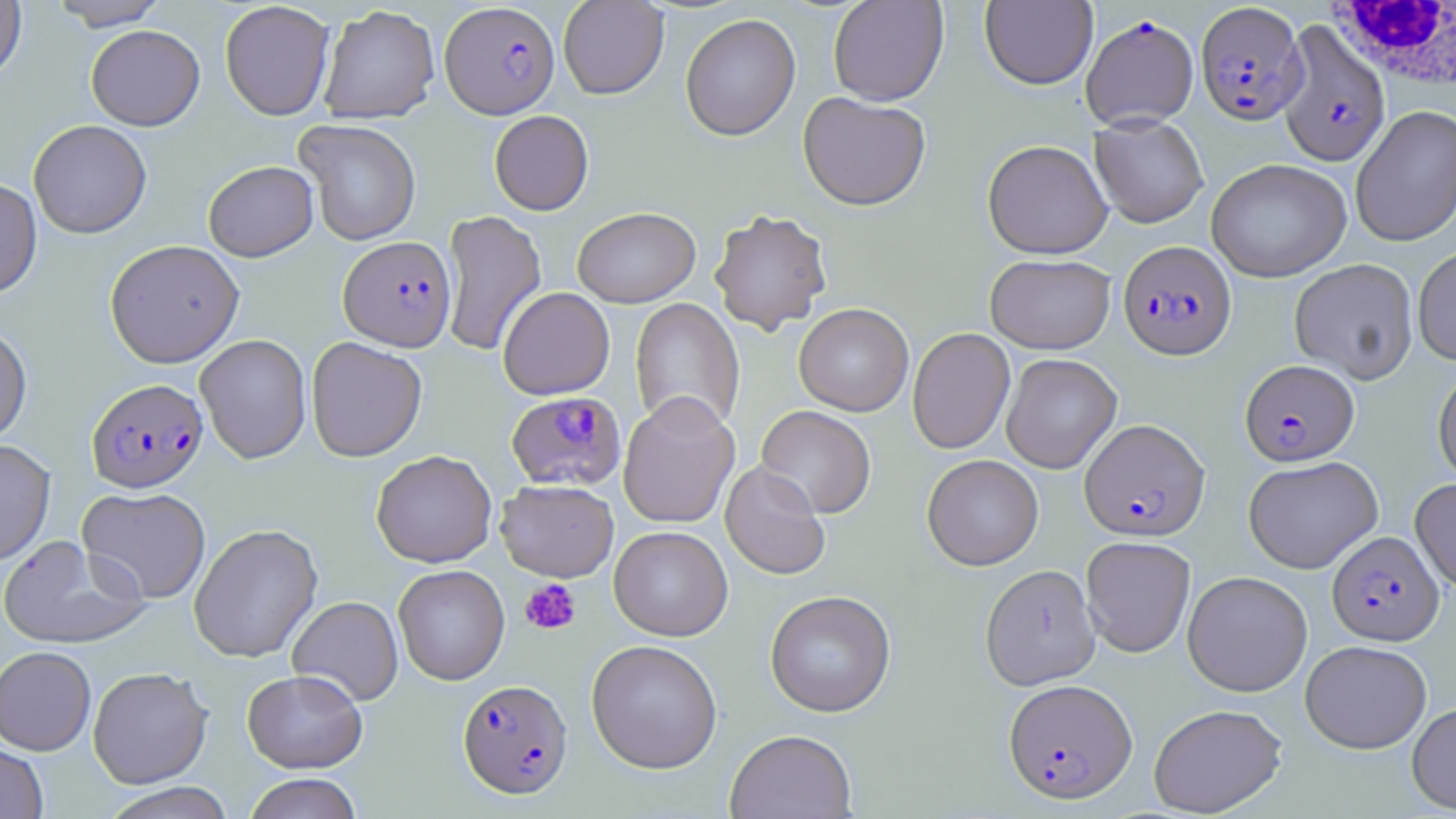
Summary:
  - Coordinate format: approximate bounding boxes as named x1/y1/x2/y2 corners in pixels
  - White blood cell locations: (x1=1328, y1=1, x2=1456, y2=92)
  - Plasmodium falciparum-infected red blood cell locations: (x1=440, y1=2, x2=560, y2=118), (x1=1195, y1=2, x2=1307, y2=125), (x1=1081, y1=14, x2=1199, y2=130), (x1=1276, y1=21, x2=1391, y2=167), (x1=338, y1=235, x2=456, y2=352), (x1=1118, y1=240, x2=1236, y2=359), (x1=1239, y1=359, x2=1359, y2=466), (x1=86, y1=377, x2=208, y2=492), (x1=506, y1=391, x2=626, y2=491), (x1=1079, y1=418, x2=1210, y2=541), (x1=1327, y1=531, x2=1444, y2=645), (x1=1003, y1=677, x2=1137, y2=804), (x1=457, y1=679, x2=573, y2=799)
  - Platelet locations: (x1=519, y1=578, x2=581, y2=635)
  - Uninfected red blood cell locations: (x1=48, y1=0, x2=169, y2=30), (x1=558, y1=0, x2=669, y2=99), (x1=827, y1=0, x2=948, y2=106), (x1=0, y1=1, x2=27, y2=82), (x1=219, y1=1, x2=335, y2=121), (x1=979, y1=1, x2=1098, y2=90), (x1=318, y1=4, x2=440, y2=124), (x1=680, y1=12, x2=801, y2=141), (x1=86, y1=25, x2=205, y2=130), (x1=798, y1=92, x2=931, y2=211), (x1=1350, y1=105, x2=1456, y2=248), (x1=489, y1=110, x2=594, y2=215), (x1=1090, y1=113, x2=1209, y2=228), (x1=28, y1=119, x2=152, y2=239), (x1=294, y1=119, x2=422, y2=246), (x1=982, y1=139, x2=1112, y2=259), (x1=1206, y1=158, x2=1352, y2=282), (x1=203, y1=160, x2=318, y2=261), (x1=0, y1=177, x2=42, y2=300), (x1=571, y1=206, x2=701, y2=308), (x1=709, y1=208, x2=833, y2=335), (x1=440, y1=210, x2=547, y2=356), (x1=105, y1=239, x2=244, y2=367), (x1=1412, y1=245, x2=1456, y2=365), (x1=985, y1=254, x2=1116, y2=354), (x1=1289, y1=258, x2=1419, y2=385), (x1=498, y1=287, x2=615, y2=400), (x1=629, y1=297, x2=745, y2=435), (x1=793, y1=303, x2=914, y2=416), (x1=0, y1=322, x2=33, y2=445), (x1=907, y1=328, x2=1015, y2=454), (x1=194, y1=334, x2=312, y2=464), (x1=306, y1=336, x2=427, y2=462), (x1=1000, y1=353, x2=1122, y2=474), (x1=1433, y1=366, x2=1456, y2=486), (x1=618, y1=392, x2=741, y2=529), (x1=756, y1=405, x2=876, y2=518), (x1=0, y1=439, x2=55, y2=566), (x1=371, y1=449, x2=497, y2=568), (x1=922, y1=454, x2=1043, y2=571), (x1=1243, y1=455, x2=1383, y2=574), (x1=719, y1=460, x2=831, y2=581), (x1=1410, y1=478, x2=1456, y2=591), (x1=495, y1=479, x2=619, y2=582), (x1=77, y1=486, x2=211, y2=604), (x1=189, y1=523, x2=323, y2=663), (x1=608, y1=526, x2=733, y2=641), (x1=0, y1=534, x2=151, y2=650), (x1=1080, y1=535, x2=1196, y2=657), (x1=393, y1=564, x2=509, y2=685), (x1=980, y1=564, x2=1100, y2=691), (x1=1182, y1=570, x2=1313, y2=697), (x1=765, y1=589, x2=896, y2=717), (x1=287, y1=595, x2=403, y2=706), (x1=586, y1=639, x2=722, y2=773), (x1=1300, y1=640, x2=1432, y2=754), (x1=0, y1=646, x2=97, y2=755), (x1=87, y1=666, x2=213, y2=788), (x1=242, y1=669, x2=368, y2=773), (x1=1407, y1=700, x2=1456, y2=814), (x1=1148, y1=703, x2=1287, y2=817), (x1=724, y1=729, x2=857, y2=818), (x1=0, y1=742, x2=49, y2=819), (x1=242, y1=773, x2=364, y2=819), (x1=99, y1=782, x2=238, y2=819)
  - Slide-level diagnosis: Plasmodium falciparum
  - Stain: May-Grünwald-Giemsa
  - Field of view: one of a larger specimen
  - Magnification: 1000x
  - Image size: 1456×819 pixels
  - Preparation: thin blood film
  - Modality: light microscopy